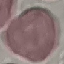
Result: no malaria parasites detected. Automatically extracted cell patch, resized to 64 × 64 pixels. Giemsa-stained preparation. Photographed with a smartphone camera at the microscope eyepiece. Thin blood film.